Give the extent of all uninfected red blood cells.
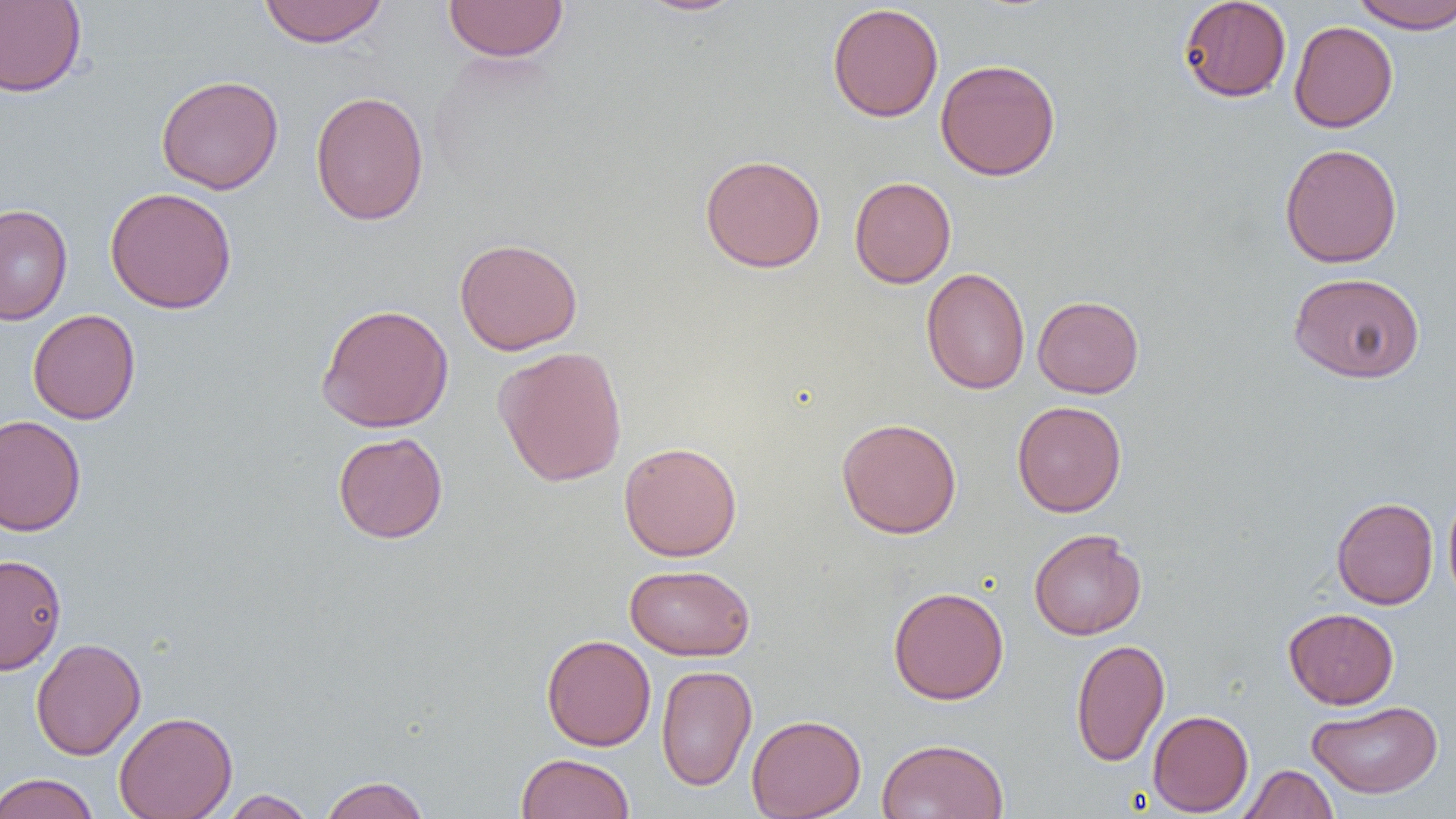
Approximate bounding boxes as (x1, y1, x2, y2) in pixels.
Uninfected red blood cells: (258, 0, 390, 47), (635, 0, 748, 17), (1178, 0, 1292, 103), (1350, 0, 1456, 33), (0, 1, 86, 97), (443, 1, 569, 62), (827, 3, 944, 122), (1289, 20, 1398, 133), (935, 58, 1061, 181), (156, 74, 284, 195), (310, 91, 429, 226), (1279, 143, 1403, 268), (699, 154, 826, 273), (849, 176, 956, 288), (105, 186, 237, 314), (0, 203, 73, 324), (454, 237, 583, 355), (921, 267, 1031, 394), (1288, 271, 1425, 383), (1032, 295, 1144, 398), (316, 303, 454, 432), (28, 308, 141, 424), (493, 345, 628, 487), (1012, 400, 1127, 517), (0, 414, 87, 537), (836, 417, 963, 539), (333, 431, 448, 544), (618, 441, 743, 561), (1443, 485, 1456, 610), (1331, 497, 1439, 609), (1028, 529, 1147, 640), (0, 553, 67, 675), (624, 564, 755, 661), (888, 586, 1009, 705), (1283, 607, 1399, 709), (541, 633, 657, 751), (30, 637, 146, 761), (1070, 638, 1170, 766), (656, 664, 757, 792), (1308, 700, 1443, 798), (1147, 709, 1254, 816), (114, 711, 238, 819), (746, 714, 866, 819), (876, 738, 1010, 819), (516, 752, 635, 819), (1239, 764, 1339, 819), (0, 772, 99, 818), (319, 775, 430, 819), (220, 789, 317, 818).

slide_level_diagnosis: negative for blood parasites
modality: light microscopy
image_size: 1456×819 pixels
magnification: 1000x
field_of_view: one of a larger specimen
preparation: thin blood smear